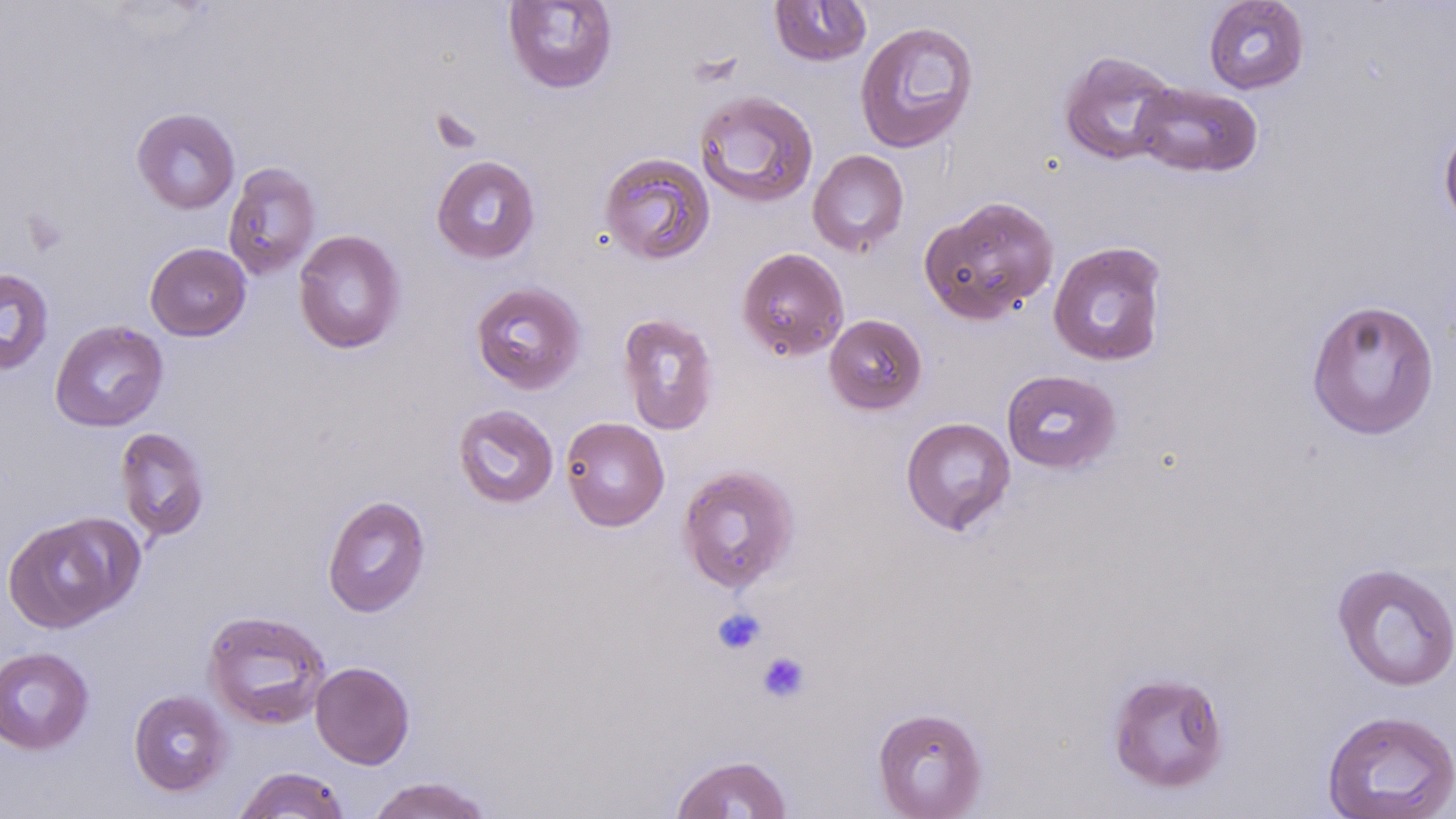 Approximate bounding boxes as named x1/y1/x2/y2 corners in pixels. Platelet locations: (x1=711, y1=607, x2=766, y2=655), (x1=755, y1=650, x2=811, y2=704). Uninfected red blood cell locations: (x1=769, y1=0, x2=871, y2=67), (x1=1203, y1=0, x2=1310, y2=94), (x1=503, y1=1, x2=618, y2=94), (x1=854, y1=20, x2=979, y2=153), (x1=1058, y1=50, x2=1180, y2=166), (x1=1132, y1=82, x2=1263, y2=178), (x1=694, y1=90, x2=819, y2=208), (x1=131, y1=107, x2=240, y2=214), (x1=1439, y1=121, x2=1456, y2=234), (x1=807, y1=149, x2=909, y2=256), (x1=598, y1=152, x2=715, y2=265), (x1=431, y1=154, x2=540, y2=264), (x1=223, y1=162, x2=321, y2=279), (x1=920, y1=195, x2=1059, y2=325), (x1=293, y1=228, x2=406, y2=355), (x1=1048, y1=241, x2=1168, y2=367), (x1=145, y1=242, x2=251, y2=341), (x1=737, y1=247, x2=849, y2=361), (x1=0, y1=267, x2=54, y2=376), (x1=470, y1=281, x2=587, y2=394), (x1=1305, y1=298, x2=1439, y2=440), (x1=617, y1=312, x2=720, y2=436), (x1=824, y1=314, x2=927, y2=415), (x1=50, y1=320, x2=169, y2=432), (x1=1000, y1=369, x2=1121, y2=474), (x1=453, y1=404, x2=559, y2=509), (x1=560, y1=416, x2=670, y2=532), (x1=901, y1=416, x2=1016, y2=535), (x1=114, y1=426, x2=211, y2=542), (x1=677, y1=465, x2=800, y2=593), (x1=322, y1=495, x2=431, y2=617), (x1=2, y1=513, x2=141, y2=633), (x1=1331, y1=561, x2=1456, y2=692), (x1=202, y1=609, x2=332, y2=729), (x1=0, y1=646, x2=94, y2=755), (x1=310, y1=661, x2=415, y2=769), (x1=1106, y1=671, x2=1230, y2=794), (x1=129, y1=690, x2=232, y2=796), (x1=872, y1=706, x2=988, y2=818), (x1=1321, y1=709, x2=1456, y2=819), (x1=671, y1=754, x2=793, y2=818), (x1=233, y1=767, x2=350, y2=818), (x1=365, y1=776, x2=496, y2=819). Slide-level diagnosis: negative for blood parasites. Image is 1456×819 pixels. May-Grünwald-Giemsa stain. Captured at 1000x magnification. Light microscopy. Single field of view. Thin blood smear.